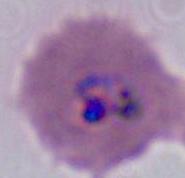

Summary:
  - Identification: Plasmodium
  - Modality: photomicrograph
  - Magnification: 400x or 1000x